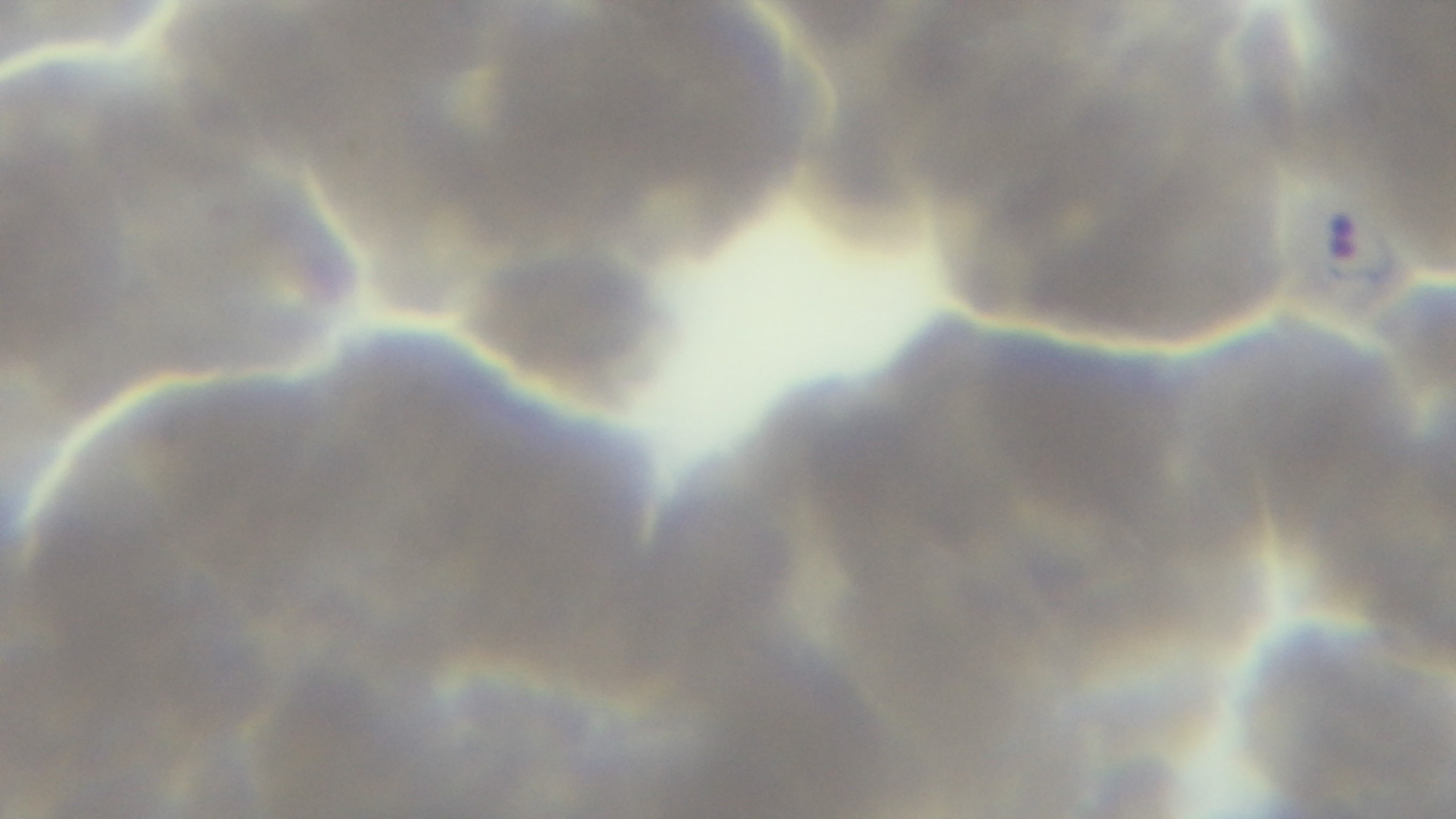
Summary:
  - Capture: mounted 4K digital camera
  - Preparation: thin smear
  - Field of view: one from the slide
  - Stain: Giemsa
  - Objective: 100x oil immersion
  - Modality: light microscopy
  - Malaria status: positive